Name the parasite shown.
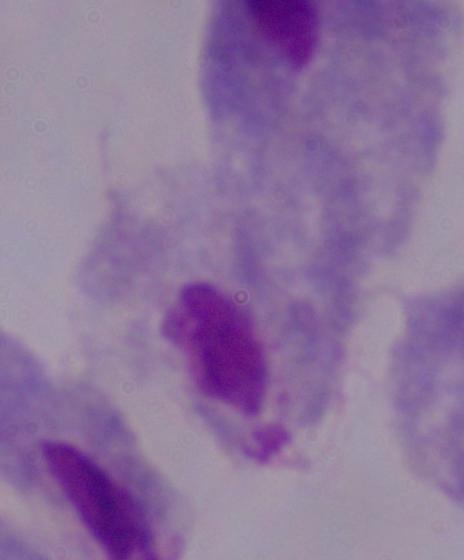

A trichomonad.

modality = photomicrograph
magnification = 1000x